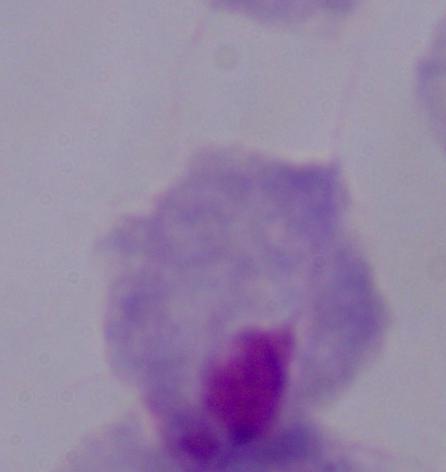
Summary:
  - Magnification: 1000x
  - Modality: micrograph
  - Identification: trichomonad